Assess this cell for malaria.
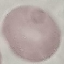

It is uninfected.

Acquired by smartphone through the microscope eyepiece. Automatically extracted cell patch, resized to 64 × 64 pixels. Giemsa-stained preparation. Thin smear of blood.